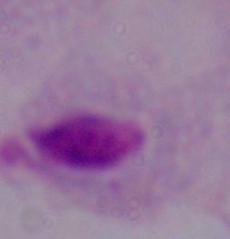

identification = trichomonad
modality = photomicrograph
magnification = 1000x